State which parasite is depicted.
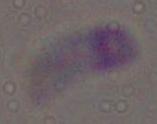
Toxoplasma gondii.

magnification: 1000x
modality: photomicrograph